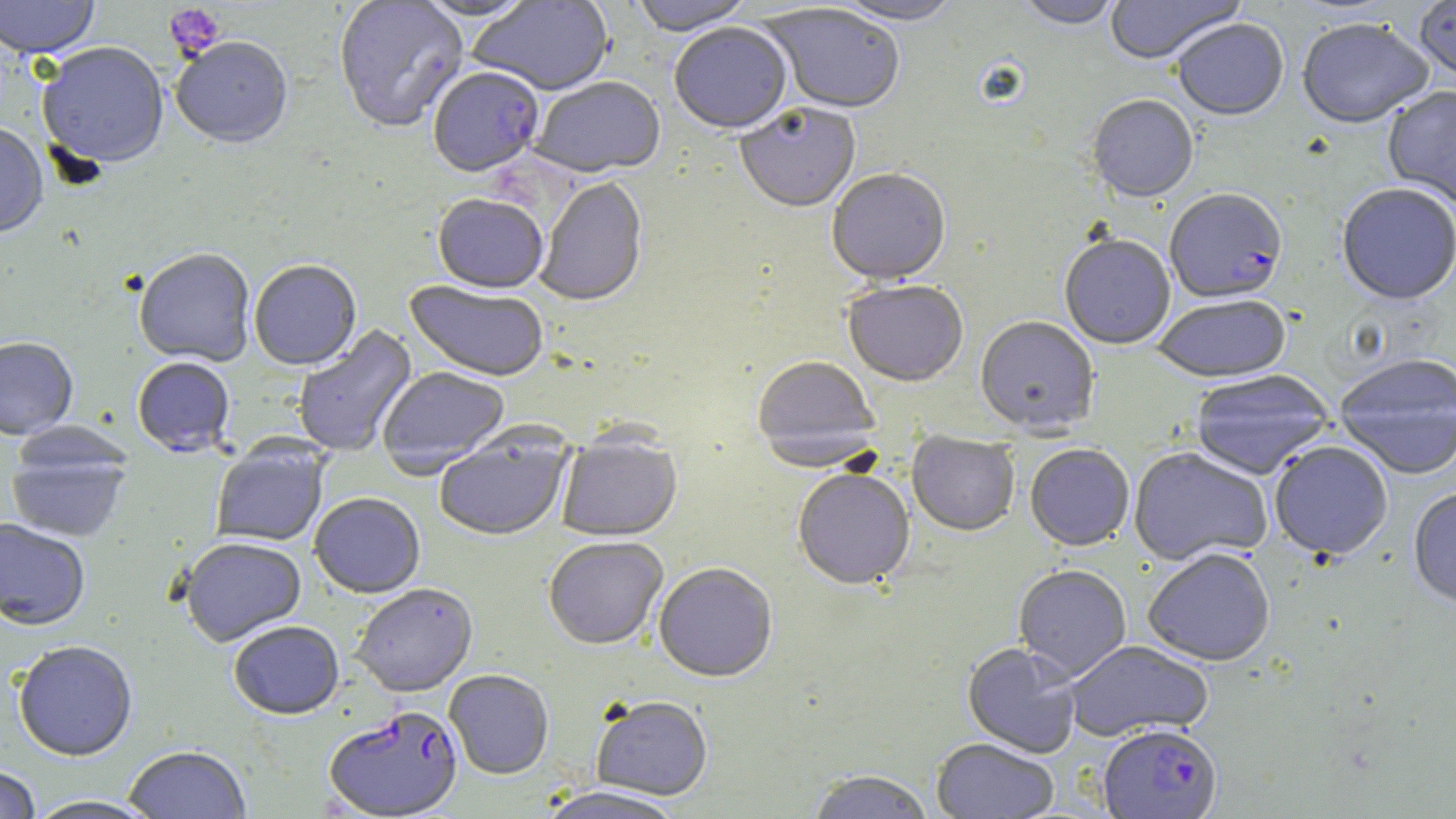
Summary:
  - Coordinate format: approximate bounding boxes as named x1/y1/x2/y2 corners in pixels
  - Plasmodium falciparum-infected red blood cell locations: (x1=428, y1=69, x2=544, y2=179), (x1=1164, y1=190, x2=1288, y2=307), (x1=324, y1=707, x2=464, y2=819), (x1=1098, y1=725, x2=1223, y2=819)
  - Uninfected red blood cell locations: (x1=0, y1=0, x2=100, y2=61), (x1=333, y1=0, x2=469, y2=135), (x1=411, y1=0, x2=541, y2=23), (x1=467, y1=0, x2=615, y2=97), (x1=631, y1=0, x2=755, y2=39), (x1=832, y1=0, x2=962, y2=28), (x1=1103, y1=0, x2=1247, y2=66), (x1=1016, y1=1, x2=1124, y2=32), (x1=1414, y1=1, x2=1456, y2=83), (x1=759, y1=6, x2=906, y2=117), (x1=1173, y1=20, x2=1288, y2=124), (x1=1297, y1=21, x2=1433, y2=132), (x1=669, y1=25, x2=792, y2=137), (x1=171, y1=39, x2=293, y2=152), (x1=37, y1=45, x2=169, y2=172), (x1=530, y1=78, x2=667, y2=181), (x1=1382, y1=87, x2=1456, y2=212), (x1=1086, y1=97, x2=1199, y2=205), (x1=735, y1=105, x2=861, y2=216), (x1=0, y1=125, x2=48, y2=240), (x1=826, y1=170, x2=951, y2=288), (x1=535, y1=178, x2=649, y2=309), (x1=1336, y1=185, x2=1455, y2=307), (x1=432, y1=196, x2=548, y2=297), (x1=1060, y1=237, x2=1175, y2=351), (x1=134, y1=250, x2=256, y2=369), (x1=249, y1=261, x2=362, y2=372), (x1=403, y1=281, x2=548, y2=383), (x1=843, y1=283, x2=969, y2=389), (x1=1152, y1=297, x2=1291, y2=384), (x1=975, y1=318, x2=1099, y2=437), (x1=293, y1=324, x2=419, y2=458), (x1=0, y1=339, x2=78, y2=441), (x1=1335, y1=357, x2=1456, y2=481), (x1=751, y1=358, x2=881, y2=472), (x1=132, y1=359, x2=235, y2=459), (x1=377, y1=368, x2=510, y2=479), (x1=1190, y1=372, x2=1335, y2=481), (x1=434, y1=425, x2=575, y2=543), (x1=556, y1=432, x2=682, y2=543), (x1=907, y1=432, x2=1020, y2=538), (x1=6, y1=436, x2=131, y2=544), (x1=211, y1=440, x2=329, y2=547), (x1=1269, y1=442, x2=1394, y2=562), (x1=1025, y1=446, x2=1134, y2=552), (x1=1129, y1=449, x2=1272, y2=567), (x1=792, y1=471, x2=915, y2=592), (x1=1407, y1=488, x2=1456, y2=612), (x1=309, y1=494, x2=425, y2=600), (x1=0, y1=519, x2=90, y2=633), (x1=544, y1=538, x2=668, y2=652), (x1=180, y1=539, x2=306, y2=648), (x1=1143, y1=550, x2=1275, y2=668), (x1=653, y1=565, x2=778, y2=685), (x1=1013, y1=566, x2=1132, y2=682), (x1=351, y1=585, x2=478, y2=699), (x1=228, y1=622, x2=344, y2=721), (x1=1064, y1=641, x2=1213, y2=743), (x1=14, y1=642, x2=138, y2=763), (x1=962, y1=642, x2=1082, y2=759), (x1=444, y1=670, x2=554, y2=780), (x1=591, y1=697, x2=713, y2=801), (x1=931, y1=739, x2=1058, y2=818), (x1=124, y1=747, x2=252, y2=819), (x1=0, y1=767, x2=41, y2=819), (x1=807, y1=772, x2=935, y2=819), (x1=535, y1=787, x2=687, y2=819), (x1=24, y1=797, x2=163, y2=819)
  - Platelet locations: (x1=164, y1=3, x2=227, y2=60)
  - Slide-level diagnosis: Plasmodium falciparum
  - Stain: May-Grünwald-Giemsa
  - Image size: 1456×819 pixels
  - Preparation: thin blood film
  - Magnification: 1000x
  - Field of view: one of a larger specimen
  - Modality: optical microscopy